Point out each Plasmodium parasite and each leukocyte.
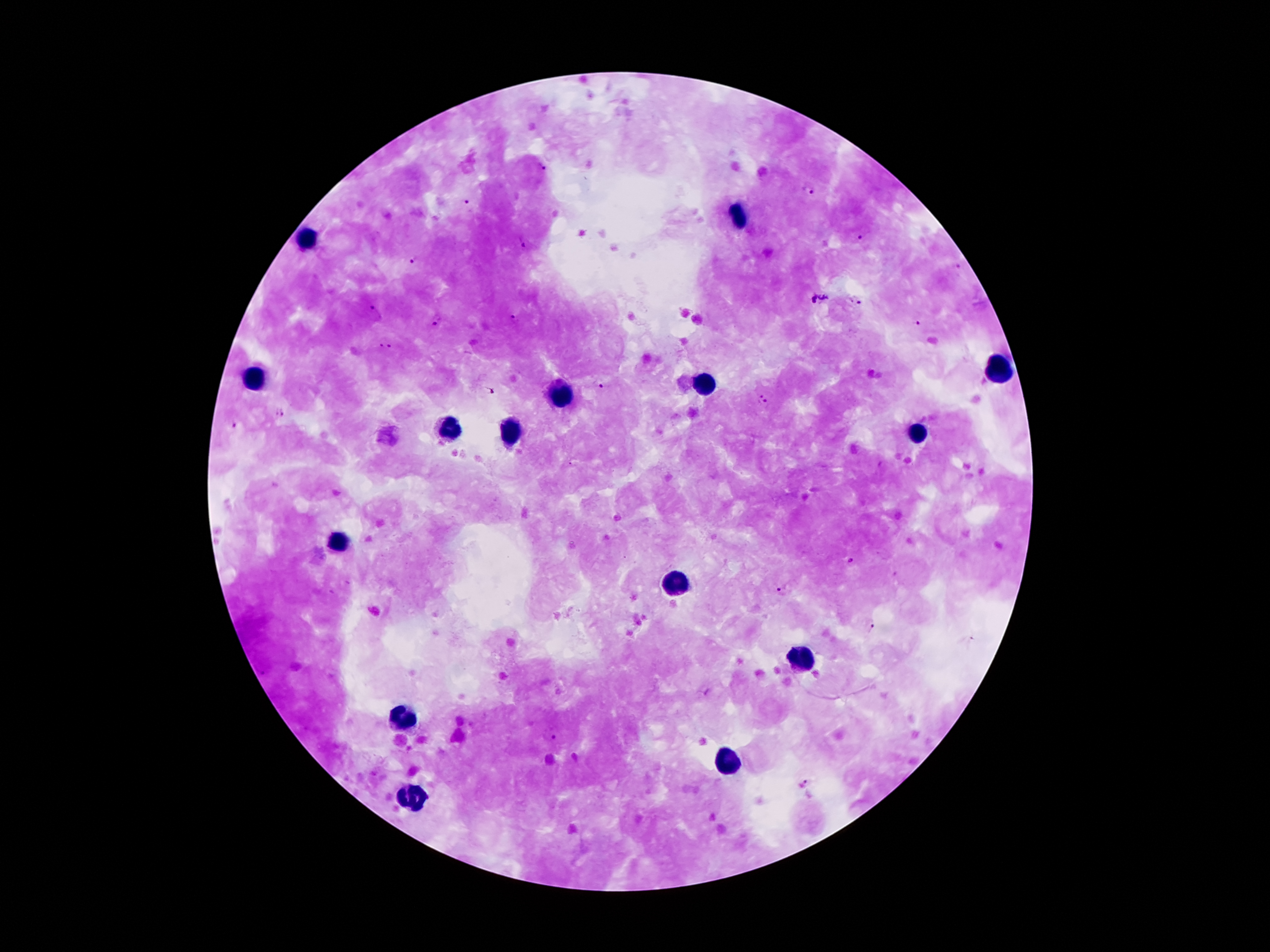
Approximate object centers, in pixels from the top-left corner.
Plasmodium parasites: (x=544, y=166), (x=808, y=189), (x=468, y=201), (x=861, y=239), (x=520, y=243), (x=414, y=259), (x=958, y=265), (x=819, y=299), (x=856, y=300), (x=377, y=311), (x=513, y=317), (x=438, y=318), (x=917, y=323), (x=387, y=346), (x=604, y=387), (x=489, y=389), (x=763, y=400), (x=279, y=415), (x=235, y=425), (x=847, y=559), (x=782, y=592), (x=873, y=628), (x=553, y=737), (x=806, y=783).
Leukocytes: (x=740, y=215), (x=304, y=241), (x=997, y=369), (x=251, y=378), (x=702, y=385), (x=563, y=397), (x=448, y=430), (x=512, y=433), (x=920, y=433), (x=340, y=544), (x=676, y=585), (x=801, y=657), (x=402, y=717), (x=724, y=763), (x=414, y=794).

image_size: 1270×952 pixels
patient_malaria_status: infected with Plasmodium falciparum
field_of_view: one from this slide
preparation: thick peripheral-blood smear
capture: smartphone through the microscope eyepiece
magnification: 100x
stain: Giemsa